Give the extent of all Babesia divergens-infected red blood cells.
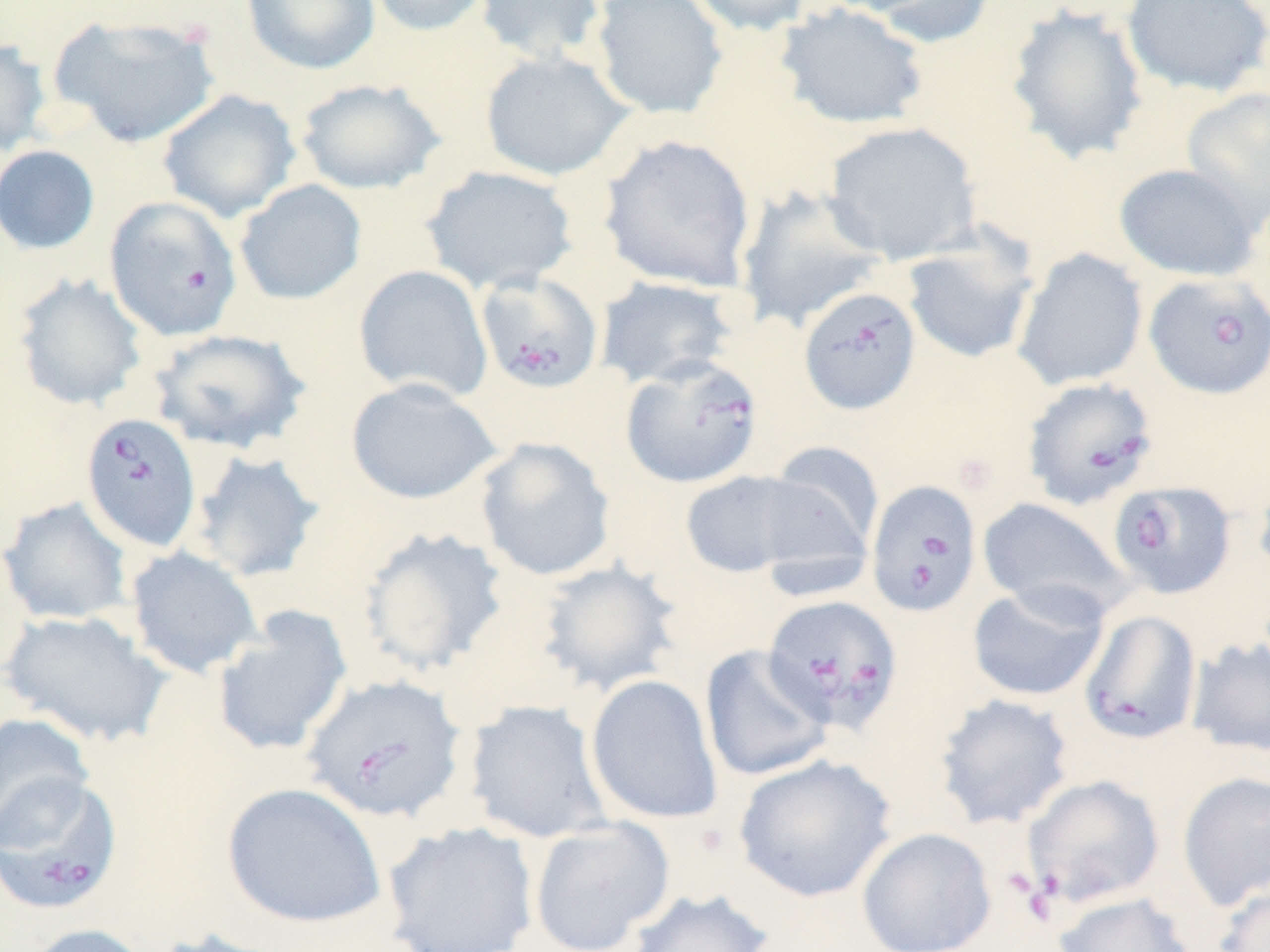
Approximate bounding boxes as [x1, y1, x2, y2] in pixels.
Babesia divergens-infected red blood cells: [104, 196, 242, 341], [474, 271, 604, 395], [1143, 272, 1270, 399], [798, 286, 921, 415], [620, 355, 763, 489], [1021, 376, 1159, 511], [80, 412, 202, 552], [866, 479, 982, 617], [1107, 479, 1235, 599], [762, 594, 903, 735], [1078, 609, 1203, 746], [301, 673, 468, 824], [0, 771, 124, 914], [1008, 774, 1165, 918].

Summary:
  - Platelet locations: [183, 17, 212, 47]
  - Uninfected red blood cell locations: [241, 0, 380, 75], [364, 0, 494, 37], [475, 0, 608, 64], [589, 0, 729, 119], [684, 0, 816, 37], [861, 0, 999, 49], [1120, 0, 1270, 99], [774, 2, 930, 130], [1005, 3, 1150, 166], [49, 14, 221, 148], [0, 37, 52, 157], [479, 49, 635, 181], [295, 78, 446, 195], [1181, 86, 1269, 229], [156, 88, 301, 223], [822, 121, 981, 264], [599, 133, 757, 292], [0, 145, 100, 255], [1113, 163, 1262, 282], [420, 164, 580, 296], [234, 179, 367, 306], [735, 185, 890, 333], [901, 233, 1040, 366], [1012, 248, 1148, 391], [353, 265, 493, 403], [12, 272, 148, 412], [593, 274, 739, 388], [148, 327, 312, 455], [346, 377, 501, 505], [474, 436, 617, 581], [764, 441, 885, 559], [187, 449, 325, 583], [1253, 463, 1270, 581], [680, 469, 825, 579], [1, 496, 134, 626], [977, 497, 1132, 620], [357, 525, 510, 678], [125, 546, 262, 679], [534, 559, 684, 697], [966, 582, 1109, 702], [211, 607, 353, 757], [1, 609, 171, 748], [1185, 637, 1270, 758], [699, 644, 834, 782], [585, 674, 723, 825], [933, 693, 1075, 831], [463, 699, 613, 844], [0, 712, 94, 847], [733, 754, 897, 903], [1176, 771, 1270, 910], [220, 781, 387, 929], [527, 817, 676, 952], [382, 821, 540, 952], [856, 827, 997, 952], [1214, 883, 1270, 951], [626, 888, 774, 952], [1051, 891, 1199, 952], [20, 923, 154, 952], [146, 927, 290, 952]
  - Slide-level diagnosis: Babesia divergens
  - Modality: light microscopy
  - Magnification: 1000x
  - Field of view: one of a larger specimen
  - Image size: 1270×952 pixels
  - Stain: May-Grünwald-Giemsa
  - Preparation: thin blood smear